Give the extent of all uninfected red blood cells.
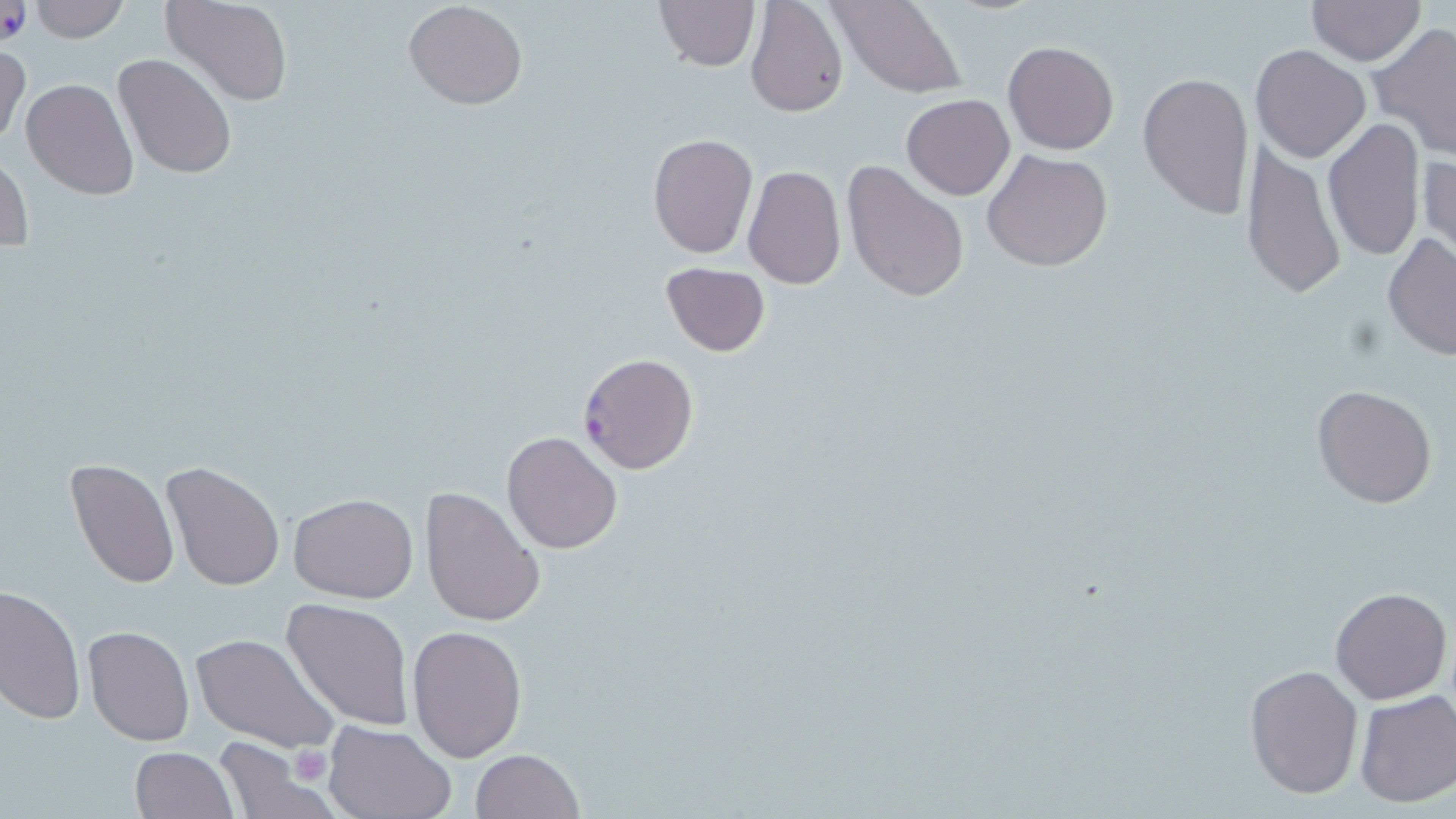

Approximate bounding boxes as (x1, y1, x2, y2) in pixels.
Uninfected red blood cells: (27, 0, 129, 42), (162, 0, 293, 107), (653, 0, 759, 70), (744, 0, 849, 118), (1307, 0, 1423, 66), (402, 1, 528, 111), (830, 1, 967, 97), (1370, 23, 1456, 161), (0, 41, 27, 151), (1003, 41, 1118, 155), (1251, 43, 1371, 164), (114, 53, 237, 179), (1346, 54, 1449, 214), (1136, 72, 1255, 221), (22, 78, 138, 201), (902, 94, 1014, 200), (1322, 117, 1424, 264), (647, 133, 759, 259), (1240, 136, 1347, 300), (982, 150, 1114, 273), (0, 151, 34, 247), (1417, 152, 1455, 277), (841, 159, 970, 304), (742, 166, 845, 291), (1381, 233, 1454, 365), (659, 262, 770, 358), (1311, 383, 1439, 509), (501, 430, 624, 554), (66, 459, 178, 588), (162, 463, 285, 592), (421, 486, 545, 629), (287, 493, 419, 604), (1, 584, 86, 725), (1330, 586, 1451, 704), (281, 597, 414, 730), (407, 624, 527, 762), (82, 625, 195, 747), (190, 633, 339, 753), (1244, 662, 1363, 799), (1353, 689, 1456, 807), (322, 720, 457, 819), (212, 737, 335, 819), (130, 747, 238, 819), (469, 749, 584, 819).

Platelet locations: (288, 746, 334, 784). Plasmodium falciparum-infected red blood cell locations: (577, 353, 700, 474). Slide-level diagnosis: Plasmodium falciparum. One field of a larger specimen. Optical microscopy. Image is 1456×819 pixels. May-Grünwald-Giemsa stain. Thin blood smear. 1000x magnification.